Identify the blood parasite species.
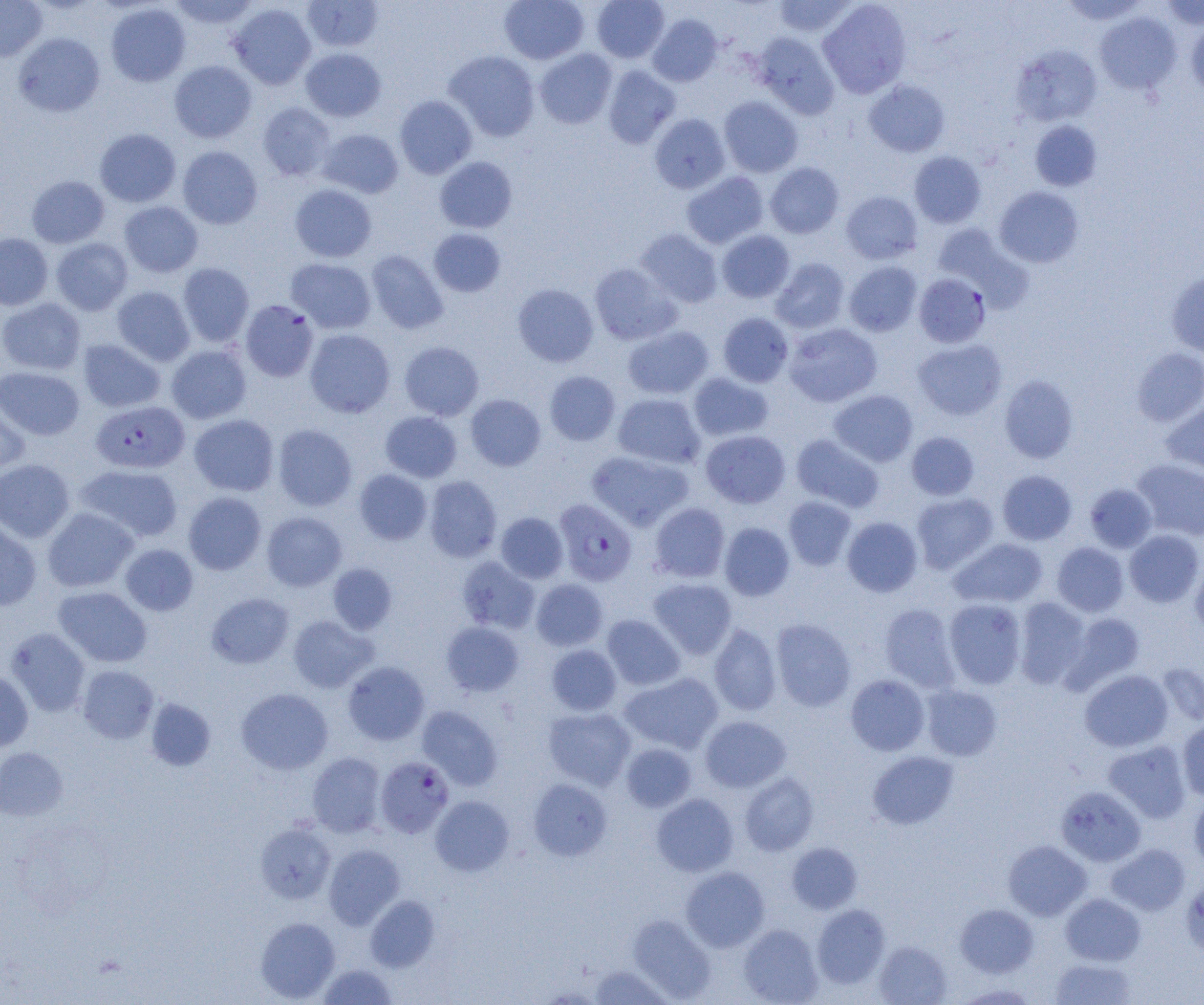
Plasmodium falciparum.

Approximate bounding boxes as [x1, y1, x2, y2] in pixels. Plasmodium falciparum-infected red blood cell locations: [914, 273, 991, 348], [240, 300, 319, 381], [91, 400, 189, 473], [554, 498, 637, 586], [375, 756, 455, 838]. Uninfected red blood cell locations: [0, 0, 47, 61], [168, 0, 259, 29], [302, 0, 383, 52], [500, 0, 589, 65], [591, 0, 669, 63], [772, 0, 859, 37], [818, 0, 911, 98], [1059, 0, 1149, 26], [1160, 0, 1204, 30], [106, 3, 191, 86], [229, 3, 316, 89], [1094, 11, 1182, 95], [647, 14, 722, 87], [1186, 19, 1204, 99], [13, 32, 105, 117], [752, 32, 840, 118], [1011, 44, 1102, 126], [301, 48, 386, 121], [534, 48, 617, 129], [444, 50, 540, 141], [169, 60, 257, 143], [602, 64, 681, 149], [864, 80, 950, 157], [395, 95, 477, 179], [719, 96, 803, 177], [258, 102, 336, 181], [649, 113, 731, 194], [1030, 120, 1102, 191], [94, 128, 181, 207], [318, 129, 404, 198], [177, 146, 263, 229], [909, 151, 986, 228], [434, 157, 517, 233], [765, 162, 844, 238], [681, 171, 768, 248], [26, 175, 109, 248], [290, 184, 377, 262], [994, 186, 1084, 268], [841, 191, 922, 264], [119, 201, 203, 277], [932, 224, 1033, 311], [428, 228, 506, 297], [635, 229, 723, 308], [717, 230, 795, 303], [0, 233, 53, 309], [51, 238, 133, 315], [365, 250, 448, 334], [286, 258, 376, 333], [771, 258, 850, 333], [844, 260, 922, 337], [589, 262, 681, 345], [177, 263, 254, 347], [1167, 270, 1204, 358], [512, 284, 599, 367], [112, 286, 195, 366], [0, 298, 86, 375], [718, 312, 794, 387], [784, 323, 882, 407], [622, 325, 714, 399], [305, 329, 395, 417], [913, 338, 1007, 421], [77, 339, 165, 412], [399, 341, 484, 420], [166, 345, 251, 424], [1132, 348, 1204, 427], [0, 366, 84, 440], [544, 370, 620, 446], [688, 372, 774, 441], [999, 375, 1078, 463], [829, 390, 918, 466], [612, 393, 705, 469], [465, 394, 546, 471], [0, 396, 30, 479], [1161, 403, 1204, 478], [380, 411, 462, 482], [189, 414, 279, 496], [273, 424, 357, 511], [701, 430, 790, 508], [906, 431, 979, 500], [792, 434, 884, 512], [587, 450, 692, 530], [0, 459, 75, 542], [1131, 459, 1204, 541], [75, 464, 183, 543], [354, 469, 432, 545], [997, 470, 1077, 545], [424, 476, 502, 562], [1084, 483, 1157, 553], [183, 492, 266, 575], [912, 492, 999, 574], [783, 496, 857, 571], [649, 502, 730, 582], [42, 507, 138, 592], [262, 512, 347, 591], [496, 512, 568, 583], [842, 516, 923, 597], [0, 518, 42, 611], [719, 522, 795, 601], [1124, 530, 1203, 607], [949, 537, 1048, 608], [1052, 542, 1128, 617], [120, 544, 198, 616], [457, 556, 539, 634], [1190, 558, 1204, 638], [327, 563, 397, 634], [649, 577, 737, 659], [531, 579, 608, 651], [53, 586, 152, 667], [207, 592, 294, 668], [943, 598, 1026, 689], [1013, 598, 1091, 689], [879, 603, 960, 692], [1062, 612, 1145, 692], [602, 614, 685, 690], [288, 615, 377, 692], [771, 618, 856, 711], [441, 621, 524, 697], [709, 623, 781, 716], [5, 628, 90, 717], [547, 644, 622, 716], [343, 661, 430, 745], [1157, 663, 1204, 727], [78, 665, 159, 743], [1079, 669, 1173, 752], [0, 671, 34, 751], [620, 672, 723, 754], [846, 675, 930, 756], [921, 685, 1002, 761], [236, 687, 333, 774], [145, 698, 216, 771], [417, 705, 503, 790], [543, 707, 636, 790], [701, 716, 791, 792], [1178, 720, 1204, 801], [1103, 740, 1191, 823], [621, 743, 696, 812], [0, 747, 68, 820], [868, 751, 958, 829], [307, 752, 386, 837], [740, 772, 819, 856], [527, 778, 612, 861], [1057, 786, 1147, 866], [1190, 793, 1204, 871], [651, 794, 738, 876], [430, 796, 514, 876], [256, 823, 335, 903], [1003, 840, 1092, 920], [786, 842, 862, 914], [323, 844, 405, 929], [1106, 844, 1190, 916], [680, 866, 770, 952], [1180, 877, 1204, 958], [1060, 893, 1145, 965], [365, 895, 440, 972], [812, 904, 890, 988], [955, 904, 1038, 977], [628, 915, 716, 1002], [255, 917, 340, 1002], [739, 924, 823, 1005], [874, 940, 951, 1004], [1050, 957, 1137, 1004], [318, 963, 397, 1005], [589, 964, 673, 1004], [952, 984, 1039, 1004]. Image is 1204×1005 pixels. Single field of view. Captured at 1000x magnification. Thin blood film. Optical microscopy.